Locate every Plasmodium parasite.
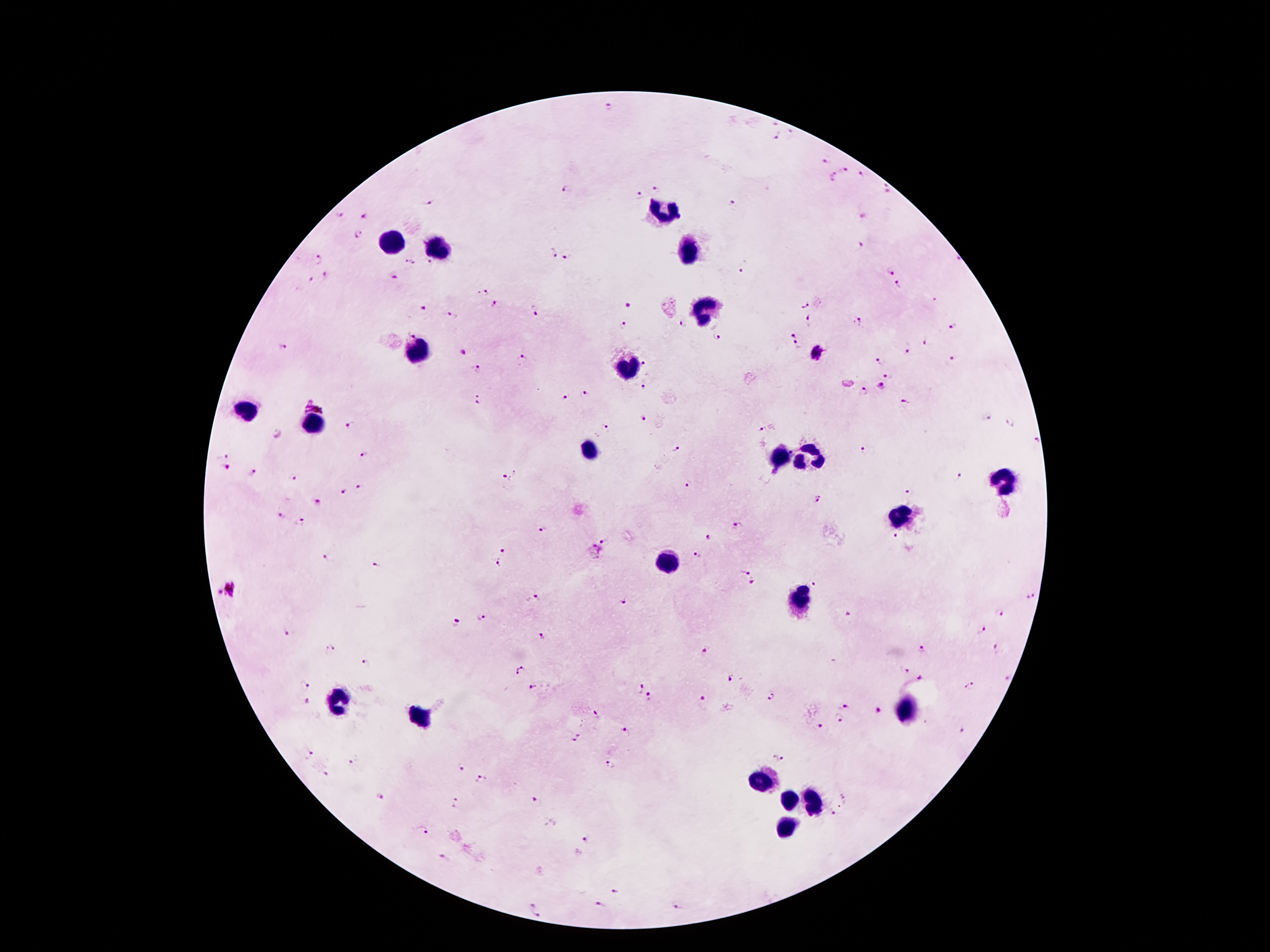

Approximate centers as {x, y} in pixels.
Plasmodium parasites: {608, 107}, {774, 123}, {792, 132}, {775, 139}, {825, 160}, {844, 171}, {861, 176}, {835, 177}, {884, 184}, {564, 189}, {658, 189}, {888, 194}, {640, 195}, {429, 200}, {732, 204}, {340, 215}, {365, 217}, {358, 234}, {860, 245}, {554, 253}, {567, 255}, {316, 258}, {958, 259}, {411, 260}, {430, 261}, {741, 272}, {891, 272}, {327, 276}, {395, 276}, {311, 281}, {897, 285}, {483, 294}, {935, 300}, {803, 303}, {499, 305}, {628, 307}, {423, 309}, {536, 311}, {449, 316}, {810, 319}, {857, 322}, {683, 323}, {625, 325}, {953, 327}, {413, 331}, {793, 332}, {718, 337}, {926, 344}, {797, 345}, {906, 348}, {282, 350}, {462, 353}, {816, 353}, {953, 357}, {521, 358}, {880, 361}, {644, 365}, {478, 369}, {888, 375}, {882, 386}, {644, 388}, {863, 391}, {583, 395}, {566, 397}, {478, 398}, {904, 401}, {316, 403}, {985, 417}, {644, 420}, {1010, 422}, {351, 425}, {606, 428}, {761, 432}, {278, 433}, {1035, 438}, {676, 449}, {864, 450}, {223, 452}, {792, 453}, {365, 456}, {226, 469}, {253, 473}, {292, 478}, {957, 478}, {504, 479}, {689, 483}, {361, 487}, {908, 490}, {345, 493}, {818, 500}, {318, 502}, {280, 515}, {302, 523}, {737, 524}, {543, 531}, {709, 537}, {896, 537}, {605, 540}, {503, 550}, {696, 555}, {330, 558}, {376, 565}, {498, 566}, {745, 569}, {752, 583}, {814, 583}, {227, 590}, {1032, 595}, {535, 598}, {624, 600}, {1001, 611}, {849, 615}, {481, 618}, {456, 623}, {981, 629}, {287, 632}, {540, 638}, {330, 648}, {920, 648}, {704, 651}, {998, 651}, {365, 664}, {906, 669}, {520, 671}, {730, 678}, {921, 679}, {1006, 679}, {303, 686}, {531, 687}, {638, 687}, {970, 688}, {771, 696}, {650, 698}, {309, 701}, {701, 701}, {844, 704}, {880, 712}, {595, 717}, {838, 718}, {820, 725}, {964, 729}, {626, 733}, {577, 739}, {310, 754}, {779, 757}, {351, 763}, {611, 765}, {458, 766}, {327, 774}, {479, 777}, {380, 796}, {845, 796}, {536, 799}, {457, 801}, {842, 806}, {832, 813}, {422, 832}, {588, 839}, {445, 859}, {615, 889}, {531, 901}, {602, 904}, {678, 904}, {540, 914}.

Leukocyte locations: {661, 209}, {393, 244}, {435, 249}, {689, 249}, {704, 310}, {417, 350}, {626, 369}, {248, 408}, {312, 425}, {590, 449}, {808, 455}, {780, 457}, {999, 481}, {898, 516}, {668, 565}, {796, 600}, {340, 699}, {905, 708}, {417, 719}, {762, 782}, {786, 802}, {813, 806}, {783, 827}. 100x magnification. Image is 1270×952 pixels. Smartphone photograph taken through the microscope eyepiece. Single field of view. Patient malaria status: infected with Plasmodium falciparum. Thick blood smear. Giemsa-stained preparation.